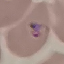
Summary:
  - Result: malaria parasites identified
  - Capture: smartphone camera at the microscope eyepiece
  - Preparation: thin smear
  - Image type: cell patch, automatically extracted from a larger field of view and resized to 64 × 64 pixels
  - Stain: Giemsa